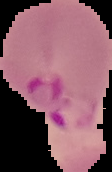 The area outside the segmented cell region is set to black. From a thin blood film. Image is 112×172 pixels. Result: Plasmodium parasites identified.